Comment on the morphology of the red blood cells.
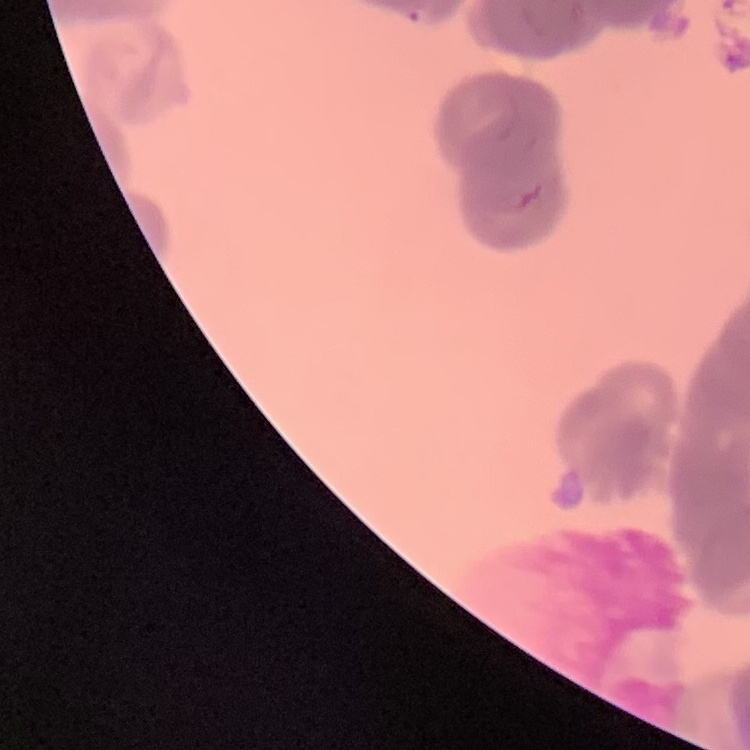

They show rouleaux formation.

stain = Field's or Giemsa
image type = square crop of a larger photomicrograph
preparation = thin blood film